Locate and identify every blood parasite.
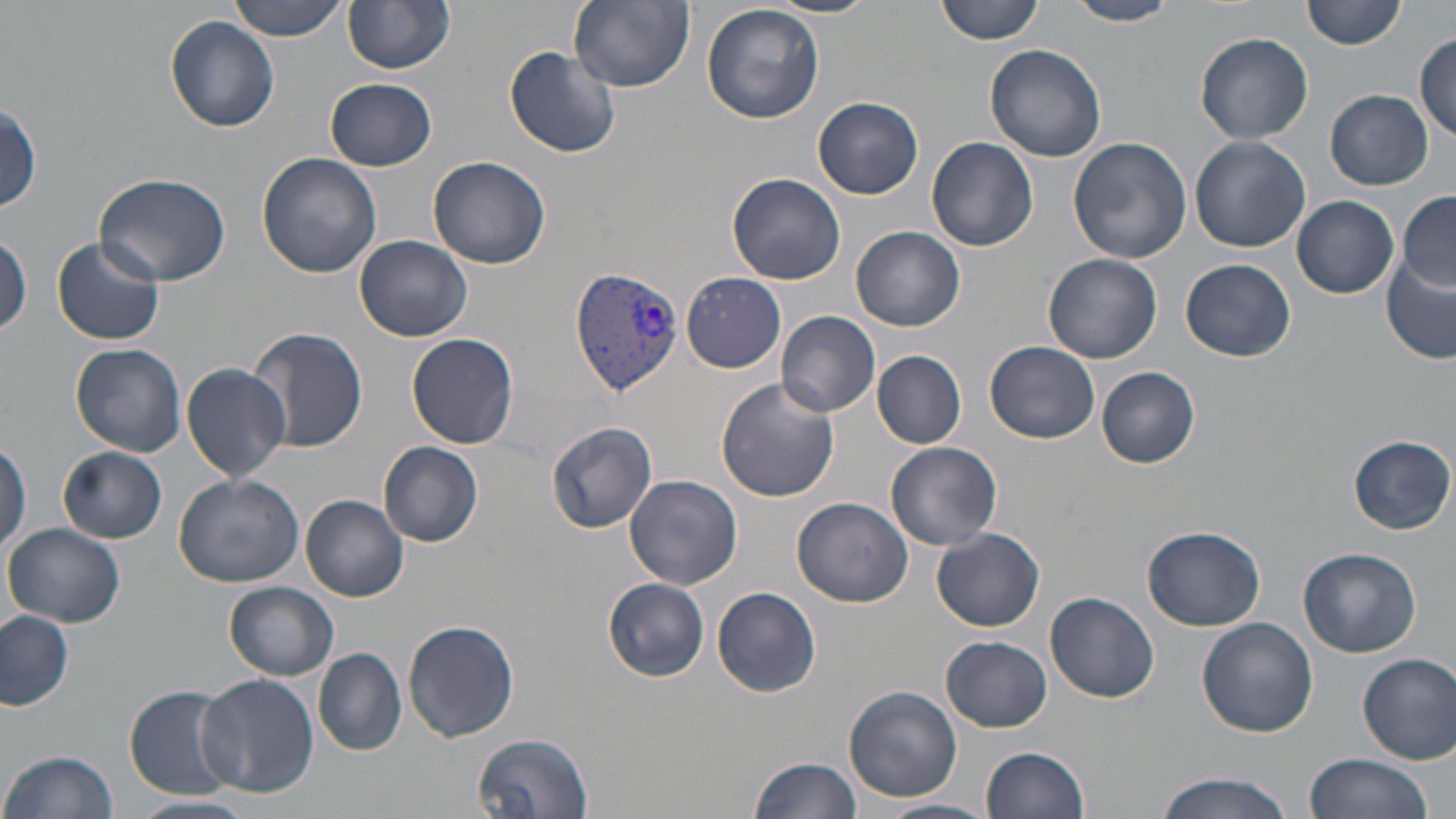

Approximate bounding boxes as (x1,y1)-(x2,y2) corner pairs in pixels.
Plasmodium vivax-infected red blood cells: (570,264)-(685,392).
No Plasmodium falciparum, Plasmodium ovale, Plasmodium malariae, Babesia divergens, or Trypanosoma brucei observed.

Uninfected red blood cell locations: (226,0)-(351,41), (344,0)-(454,74), (568,0)-(694,92), (767,0)-(876,18), (935,0)-(1046,45), (1301,0)-(1406,50), (1064,1)-(1180,26), (701,2)-(826,124), (165,16)-(279,131), (1195,32)-(1314,144), (1413,35)-(1455,144), (504,45)-(622,159), (985,45)-(1108,164), (326,77)-(436,170), (1327,90)-(1432,188), (814,96)-(923,199), (1,104)-(41,214), (926,136)-(1038,252), (1189,136)-(1310,251), (1068,137)-(1192,263), (257,153)-(382,279), (429,155)-(550,269), (96,173)-(229,285), (727,173)-(846,285), (1397,189)-(1456,291), (1293,195)-(1398,299), (851,225)-(965,331), (0,233)-(32,336), (355,234)-(472,341), (51,236)-(165,347), (1044,254)-(1163,363), (1180,259)-(1296,362), (1383,259)-(1456,364), (681,272)-(786,373), (776,311)-(881,417), (250,327)-(368,453), (407,333)-(519,450), (985,341)-(1100,443), (71,343)-(189,457), (873,350)-(967,449), (181,362)-(291,482), (1097,368)-(1200,468), (715,377)-(840,502), (547,421)-(659,532), (0,435)-(32,554), (1349,435)-(1453,533), (380,441)-(483,545), (885,441)-(1003,550), (60,447)-(168,543), (174,473)-(304,587), (624,475)-(742,587), (301,495)-(408,600), (793,496)-(913,607), (3,523)-(128,629), (1143,525)-(1265,631), (932,527)-(1045,632), (1298,547)-(1421,656), (603,578)-(709,681), (224,581)-(339,680), (712,585)-(821,697), (1047,592)-(1159,704), (0,610)-(73,710), (1197,617)-(1319,736), (404,620)-(519,742), (942,636)-(1052,731), (314,647)-(406,755), (1358,653)-(1456,764), (195,674)-(318,796), (122,682)-(244,799), (843,685)-(962,802), (475,732)-(596,818), (980,746)-(1090,819), (2,749)-(118,819), (1303,753)-(1434,819), (749,755)-(864,819), (1152,769)-(1300,819), (130,793)-(257,818), (881,798)-(998,819). Slide-level diagnosis: Plasmodium vivax. Thin blood film. May-Grünwald-Giemsa stain. One field of a larger specimen. 1000x magnification. Image is 1456×819 pixels. Light microscopy.